Give the position of every Plasmodium parasite, noting whether each is a trophozoite, schizont, or gametocyte.
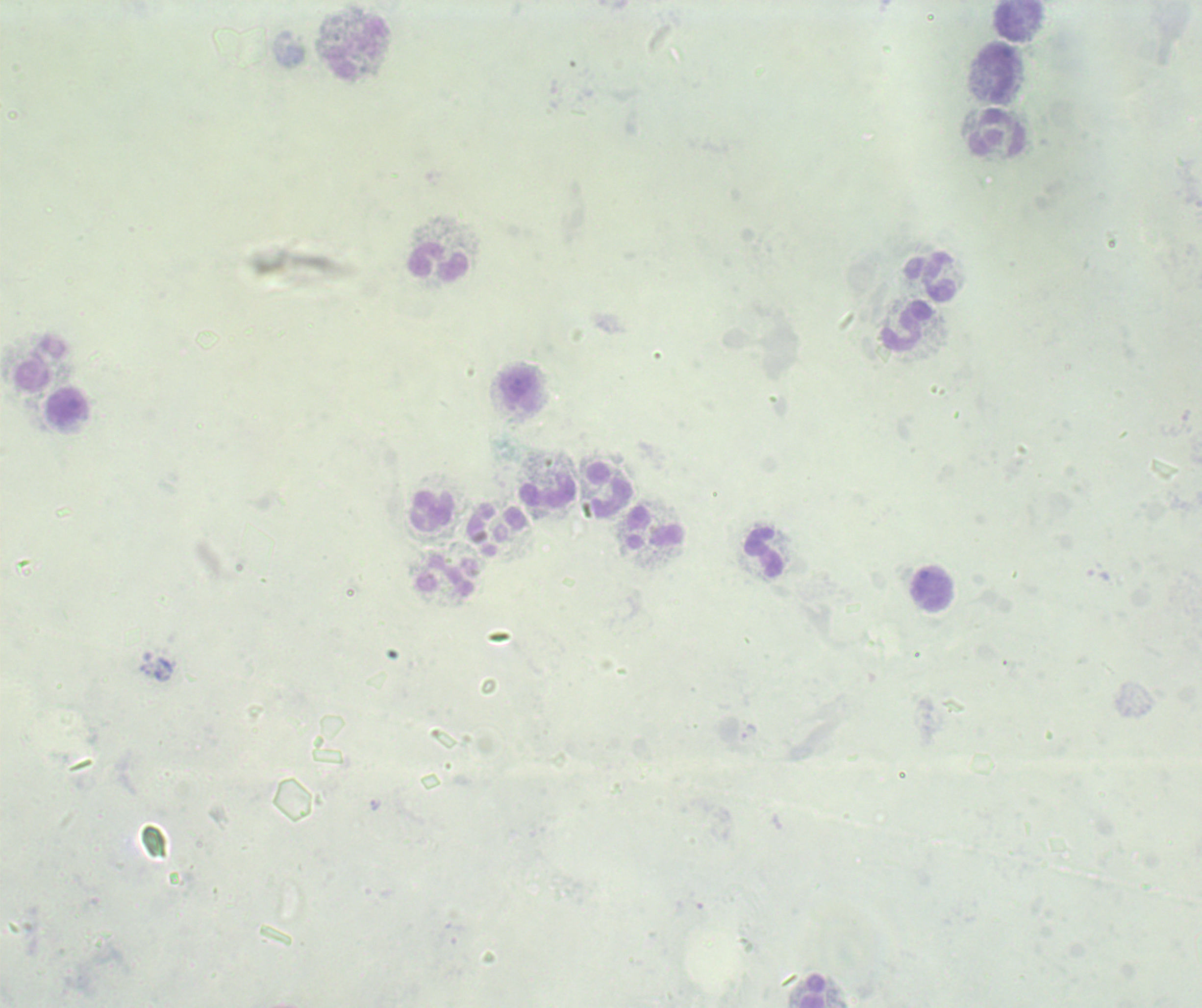

No Plasmodium parasites detected.

Approximate centers as {x, y} in pixels. Leukocyte locations: {1019, 21}, {357, 49}, {997, 72}, {998, 133}, {438, 262}, {930, 277}, {907, 326}, {40, 363}, {520, 391}, {69, 407}, {611, 489}, {547, 494}, {432, 511}, {653, 527}, {764, 553}, {446, 575}, {931, 589}, {812, 991}. Romanowsky-stained preparation. Previously used in an actual diagnosis. 100x magnification. Image is 1202×1008 pixels. Thick blood film. Background quality: poor. One field from this slide.